Assess this cell for malaria.
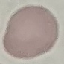
Uninfected.

Thin blood smear. Giemsa stain. Acquired by smartphone through the microscope eyepiece. Automatically extracted cell patch, resized to 64 × 64 pixels.